Report the malaria status of this cell.
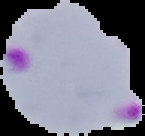

Parasitized.

Summary:
  - Image size: 145×136 pixels
  - Preparation: thin blood film
  - Image type: segmented cell region on a black background